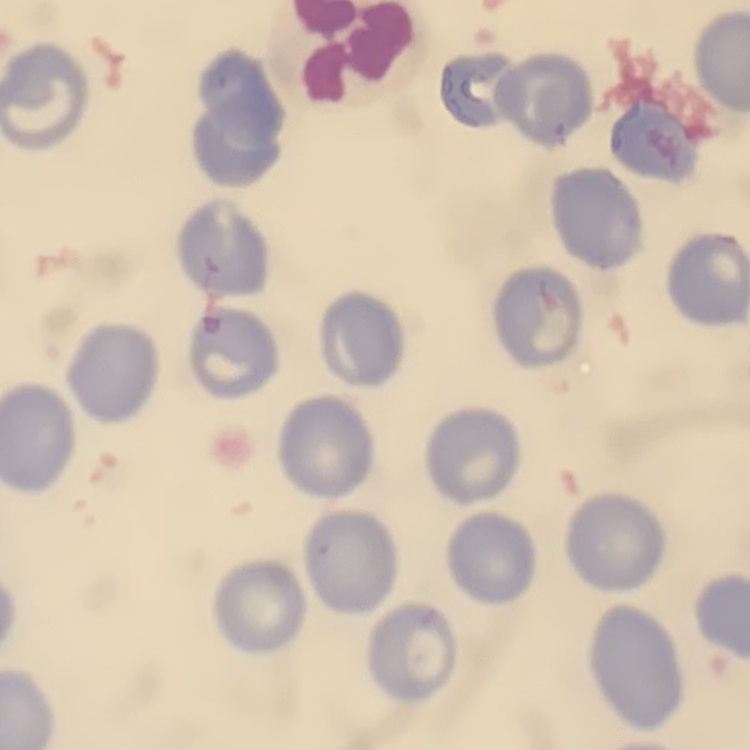
The red blood cells exhibit no rouleaux formation. One tile cut from a larger photomicrograph. Stained with either Field's or Giemsa. Thin peripheral smear.